Assess this cell for malaria.
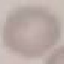

It is uninfected.

Thin smear of blood. Giemsa-stained preparation. Automatically extracted cell patch, resized to 64 × 64 pixels. Photographed with a smartphone camera at the microscope eyepiece.